Assess the morphology of the red blood cells.
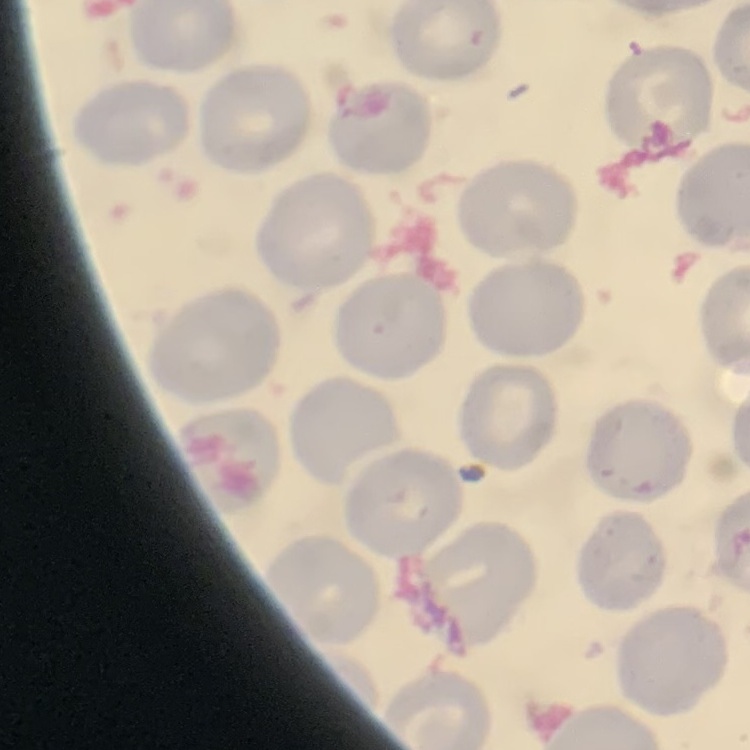

No rouleaux formation.

Summary:
  - Stain: Field's or Giemsa
  - Image type: square crop of a larger photomicrograph
  - Preparation: thin blood smear